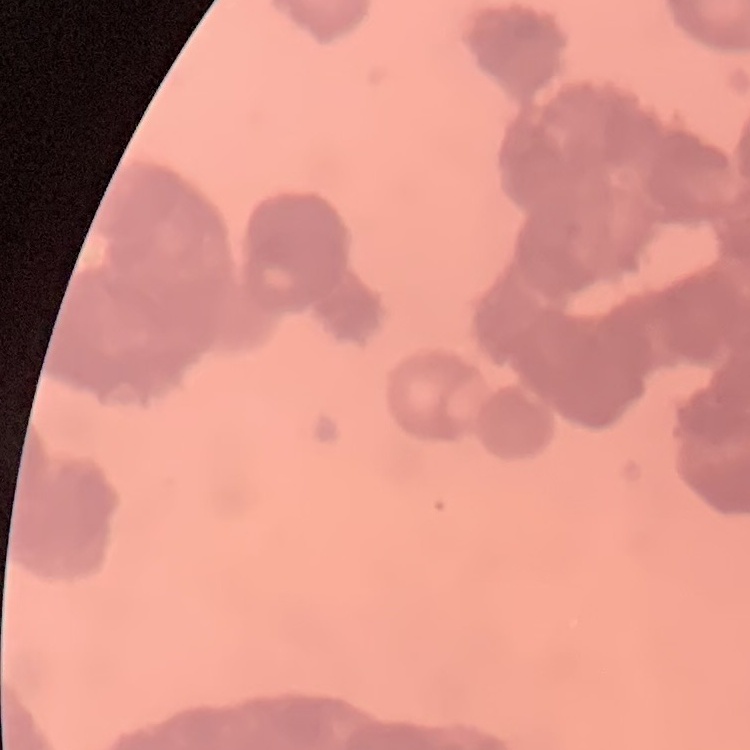
{
  "erythrocyte_morphology": "rouleaux formation",
  "stain": "Field's or Giemsa",
  "preparation": "thin blood smear",
  "image_type": "square crop of a larger photomicrograph"
}